Find the red blood cells that are infected with P. falciparum, and any of indeterminate infection status.
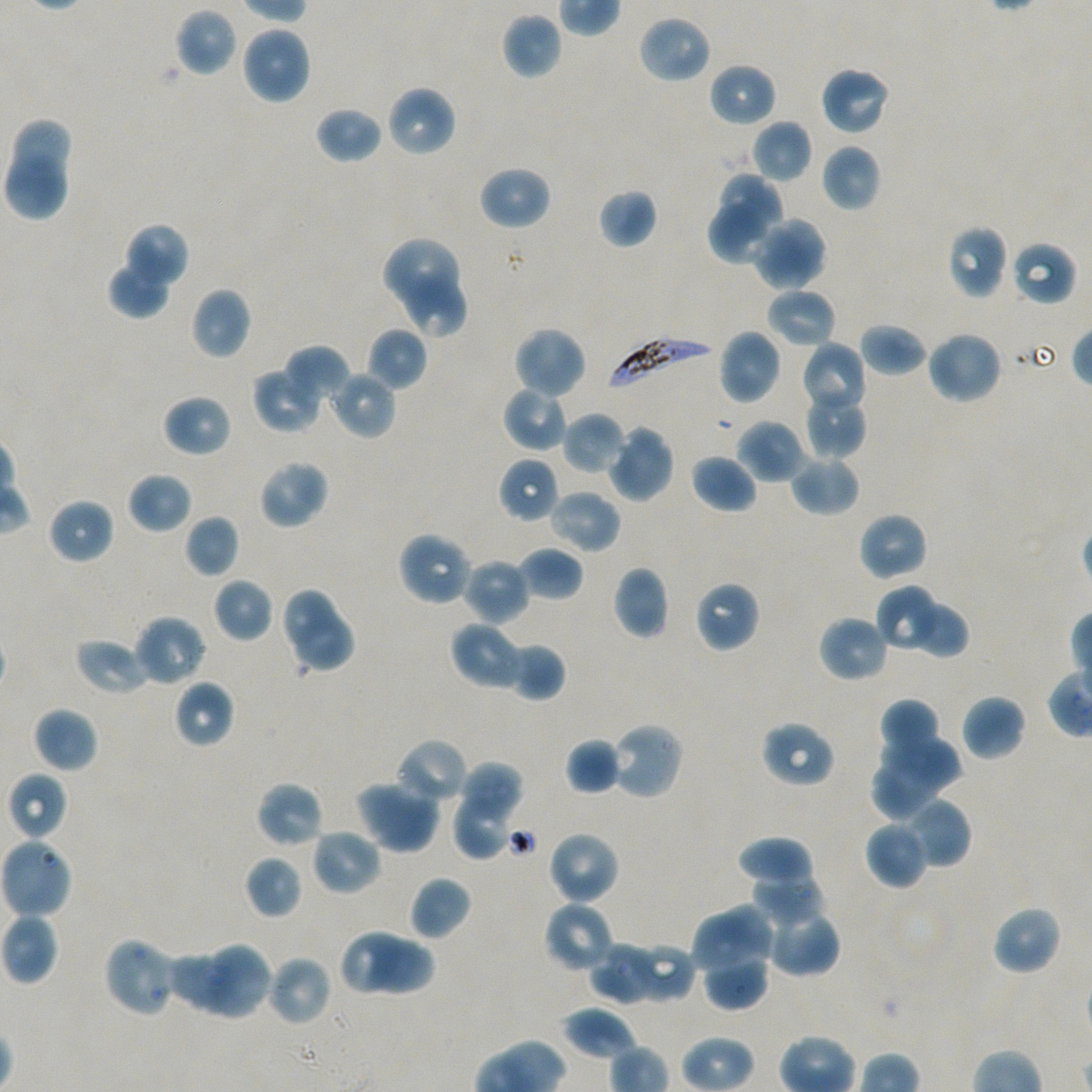
Approximate bounding boxes as [x1, y1, x2, y2] in pixels. Not every red blood cell is marked.
Infected red blood cells: [605, 334, 717, 393].
No red blood cells of indeterminate infection status observed.

locations_of_uninfected_red_blood_cells: '[174, 8, 238, 76], [501, 12, 562, 79], [637, 14, 712, 84], [240, 25, 312, 105], [708, 62, 776, 126], [820, 65, 891, 136], [385, 86, 456, 158], [314, 105, 382, 164], [12, 118, 70, 175], [750, 119, 813, 183], [820, 143, 881, 213], [5, 150, 73, 223], [478, 165, 551, 230], [722, 173, 782, 244], [598, 188, 657, 249], [708, 198, 770, 263], [769, 217, 826, 282], [122, 223, 189, 291], [946, 225, 1008, 299], [751, 227, 812, 291], [381, 238, 458, 308], [1010, 240, 1077, 306], [108, 258, 172, 320], [407, 276, 467, 338], [189, 286, 252, 360], [765, 288, 837, 348], [859, 322, 928, 376], [367, 326, 427, 391], [512, 326, 587, 399], [718, 328, 782, 405], [925, 330, 1002, 405], [799, 341, 868, 416], [284, 344, 350, 405], [251, 365, 321, 433], [329, 370, 397, 440], [503, 385, 570, 452], [804, 389, 868, 459], [162, 394, 232, 457], [562, 412, 627, 475], [736, 419, 807, 484], [606, 424, 674, 503], [690, 453, 758, 513], [789, 453, 860, 516], [498, 457, 560, 523], [258, 458, 329, 529], [128, 471, 193, 534], [548, 489, 621, 554], [46, 497, 115, 564], [858, 511, 928, 581], [184, 514, 240, 577], [397, 531, 474, 606], [517, 547, 583, 600], [460, 557, 530, 625], [613, 566, 670, 640], [212, 577, 273, 643], [694, 581, 760, 653], [280, 585, 337, 647], [875, 585, 946, 653], [907, 600, 970, 659], [295, 611, 358, 672], [132, 615, 206, 687], [817, 615, 889, 683], [450, 621, 526, 691], [74, 638, 150, 695], [505, 642, 566, 702], [173, 679, 234, 748], [960, 694, 1026, 761], [877, 697, 942, 766], [32, 706, 98, 773], [760, 720, 836, 788], [608, 721, 685, 800], [879, 737, 967, 794], [395, 738, 468, 805], [564, 738, 621, 795], [460, 761, 523, 817], [875, 761, 938, 820], [8, 771, 69, 839], [354, 780, 441, 854], [255, 781, 324, 848], [900, 797, 970, 869], [456, 801, 507, 858], [864, 820, 928, 890], [310, 829, 382, 896], [546, 830, 620, 906], [736, 837, 815, 887], [0, 838, 73, 920], [244, 854, 303, 920], [748, 867, 826, 923], [408, 875, 472, 941], [544, 901, 615, 973], [761, 902, 840, 977], [718, 903, 778, 964], [991, 905, 1062, 976], [1, 913, 60, 985], [691, 915, 761, 983], [340, 928, 418, 997], [103, 936, 179, 1019], [213, 939, 275, 1019], [369, 941, 436, 993], [626, 942, 697, 1003], [589, 943, 660, 1004], [165, 951, 242, 1013], [265, 954, 333, 1026], [702, 958, 770, 1011], [562, 1006, 636, 1059]'
donor_blood_group: A+/O+
objective: 100x, oil immersion, numerical aperture 1.45
field_of_view: one from this slide
preparation: thin blood smear
culture: P. falciparum strain NF54, static, in vitro
image_size: 1092×1092 pixels
stain: Giemsa